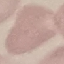
result = no malaria parasites seen
capture = smartphone through the microscope eyepiece
image type = cell patch, automatically extracted from a larger field of view and resized to 64 × 64 pixels
preparation = thin blood film
stain = Giemsa